Assess this cell for malaria.
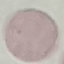
Uninfected.

Summary:
  - Preparation: thin smear
  - Image type: cell patch, automatically extracted from a larger field of view and resized to 64 × 64 pixels
  - Stain: Giemsa
  - Capture: smartphone camera at the microscope eyepiece